Name the parasite shown.
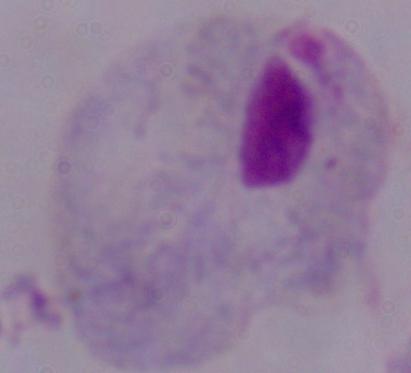

A trichomonad.

modality = micrograph
magnification = 1000x